Name the parasite shown.
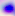

Toxoplasma gondii.

modality = photomicrograph
magnification = 400x